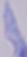
modality = micrograph
magnification = 1000x
identification = trypanosome